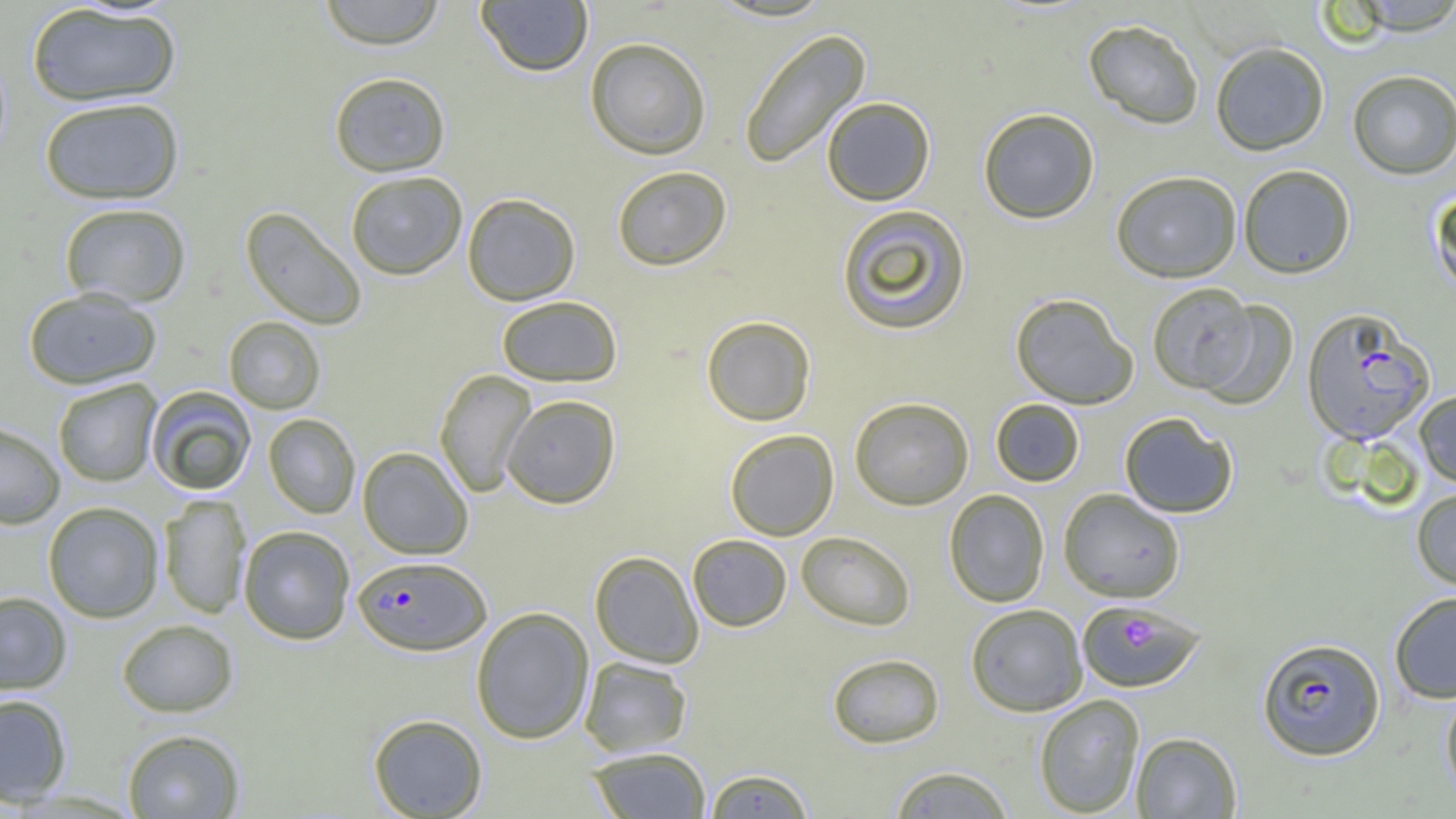
Plasmodium falciparum-infected red blood cell locations = approximate bounding boxes as named x1/y1/x2/y2 corners in pixels: (x1=1301, y1=308, x2=1436, y2=445), (x1=353, y1=555, x2=491, y2=655), (x1=1256, y1=636, x2=1386, y2=760)
slide-level diagnosis = Plasmodium falciparum
magnification = 1000x
modality = light microscopy
preparation = thin blood film
field of view = single
platelet locations = approximate bounding boxes as named x1/y1/x2/y2 corners in pixels: (x1=1122, y1=616, x2=1156, y2=648)
uninfected red blood cell locations = approximate bounding boxes as named x1/y1/x2/y2 corners in pixels: (x1=318, y1=0, x2=446, y2=50), (x1=1343, y1=0, x2=1456, y2=36), (x1=475, y1=1, x2=593, y2=77), (x1=25, y1=3, x2=182, y2=107), (x1=1083, y1=18, x2=1205, y2=129), (x1=738, y1=29, x2=871, y2=171), (x1=585, y1=37, x2=712, y2=159), (x1=1210, y1=41, x2=1330, y2=156), (x1=1347, y1=70, x2=1456, y2=179), (x1=328, y1=71, x2=451, y2=177), (x1=821, y1=96, x2=935, y2=206), (x1=39, y1=97, x2=185, y2=205), (x1=978, y1=107, x2=1100, y2=224), (x1=1238, y1=164, x2=1356, y2=278), (x1=612, y1=165, x2=732, y2=271), (x1=1111, y1=170, x2=1242, y2=283), (x1=345, y1=171, x2=467, y2=280), (x1=1428, y1=185, x2=1456, y2=297), (x1=462, y1=193, x2=581, y2=305), (x1=59, y1=202, x2=191, y2=308), (x1=836, y1=204, x2=972, y2=335), (x1=240, y1=207, x2=367, y2=330), (x1=1147, y1=282, x2=1258, y2=394), (x1=23, y1=287, x2=161, y2=390), (x1=1010, y1=293, x2=1138, y2=409), (x1=496, y1=295, x2=623, y2=387), (x1=1198, y1=300, x2=1298, y2=410), (x1=701, y1=315, x2=816, y2=426), (x1=224, y1=316, x2=326, y2=414), (x1=434, y1=369, x2=536, y2=498), (x1=52, y1=378, x2=163, y2=487), (x1=146, y1=386, x2=256, y2=496), (x1=1414, y1=389, x2=1456, y2=489), (x1=501, y1=394, x2=620, y2=508), (x1=849, y1=396, x2=974, y2=510), (x1=991, y1=399, x2=1084, y2=486), (x1=1118, y1=411, x2=1239, y2=518), (x1=263, y1=413, x2=360, y2=519), (x1=0, y1=421, x2=65, y2=529), (x1=724, y1=429, x2=839, y2=540), (x1=357, y1=446, x2=473, y2=559), (x1=1411, y1=485, x2=1456, y2=591), (x1=1058, y1=488, x2=1186, y2=602), (x1=943, y1=489, x2=1050, y2=607), (x1=158, y1=494, x2=251, y2=619), (x1=43, y1=501, x2=164, y2=623), (x1=238, y1=525, x2=355, y2=645), (x1=796, y1=531, x2=916, y2=630), (x1=687, y1=534, x2=792, y2=631), (x1=590, y1=550, x2=704, y2=668), (x1=0, y1=591, x2=72, y2=695), (x1=1388, y1=591, x2=1456, y2=704), (x1=1077, y1=601, x2=1203, y2=692), (x1=965, y1=603, x2=1088, y2=716), (x1=470, y1=607, x2=594, y2=745), (x1=116, y1=618, x2=239, y2=717), (x1=826, y1=652, x2=945, y2=748), (x1=579, y1=656, x2=693, y2=757), (x1=1440, y1=684, x2=1456, y2=804), (x1=0, y1=693, x2=72, y2=807), (x1=1033, y1=694, x2=1145, y2=817), (x1=368, y1=714, x2=488, y2=818), (x1=122, y1=729, x2=244, y2=818), (x1=1131, y1=732, x2=1242, y2=818), (x1=586, y1=747, x2=711, y2=819), (x1=887, y1=765, x2=1016, y2=818), (x1=703, y1=768, x2=815, y2=818)
image size = 1456×819 pixels